State the blood parasite species.
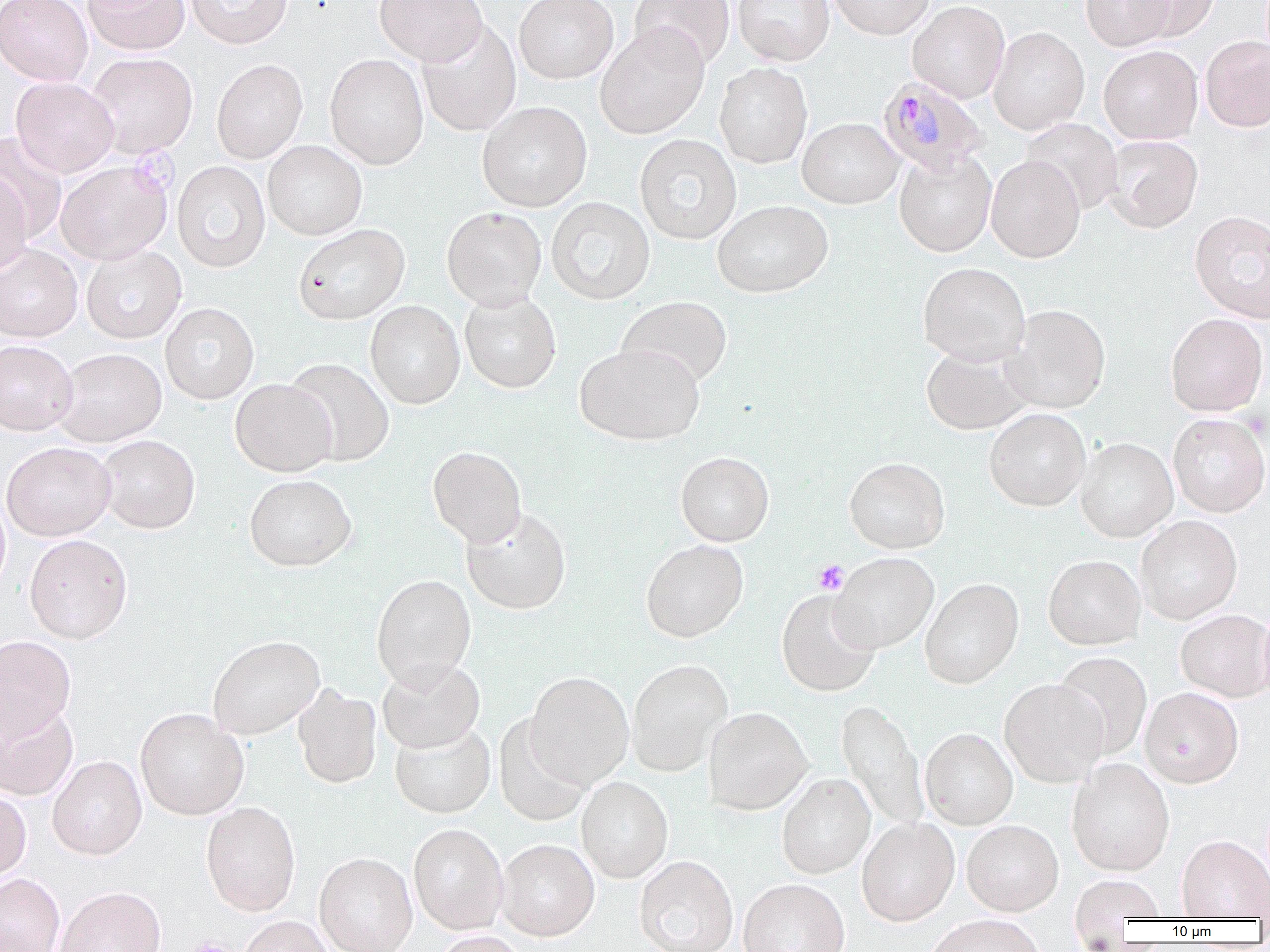

Plasmodium malariae.

Approximate bounding boxes as (x1,y1)-(x2,y2) corner pairs in pixels. Plasmodium malariae-infected red blood cell locations: (877,76)-(989,173). Uninfected red blood cell locations: (0,0)-(92,86), (83,0)-(190,55), (184,0)-(293,49), (374,0)-(488,66), (514,0)-(618,84), (630,0)-(735,70), (733,0)-(836,65), (828,0)-(934,39), (1081,0)-(1175,51), (1128,0)-(1219,42), (907,1)-(1010,104), (417,21)-(521,137), (595,25)-(709,139), (988,26)-(1089,135), (1200,35)-(1270,132), (1098,45)-(1203,144), (85,52)-(198,158), (324,54)-(429,169), (211,59)-(308,164), (714,62)-(813,169), (11,77)-(119,177), (477,101)-(592,211), (797,117)-(904,208), (1021,118)-(1123,215), (1,132)-(67,244), (634,134)-(742,245), (1103,135)-(1203,232), (262,140)-(367,240), (893,149)-(997,257), (985,155)-(1085,262), (56,161)-(172,265), (172,161)-(270,273), (0,171)-(32,277), (546,197)-(655,305), (712,200)-(833,298), (441,207)-(547,310), (1190,211)-(1270,323), (293,224)-(410,324), (0,244)-(83,342), (81,245)-(186,344), (918,262)-(1030,366), (460,291)-(562,393), (616,296)-(733,389), (365,300)-(465,409), (160,302)-(259,404), (1001,304)-(1111,413), (1165,313)-(1268,417), (0,340)-(78,435), (575,343)-(704,445), (921,345)-(1034,435), (54,348)-(166,447), (284,358)-(395,466), (229,379)-(337,477), (984,408)-(1091,511), (1168,413)-(1269,517), (96,434)-(200,533), (1076,437)-(1178,542), (1,442)-(116,540), (427,446)-(527,547), (675,451)-(774,547), (844,457)-(950,554), (244,475)-(357,572), (0,493)-(11,597), (461,506)-(572,615), (1135,515)-(1243,624), (24,534)-(133,643), (641,540)-(748,642), (830,553)-(939,653), (1043,555)-(1146,650), (371,574)-(476,690), (920,579)-(1023,688), (776,589)-(881,697), (1175,609)-(1270,702), (0,635)-(76,741), (208,635)-(325,740), (1053,651)-(1152,759), (377,658)-(485,753), (626,659)-(734,776), (525,671)-(634,788), (999,678)-(1109,788), (292,684)-(383,788), (1139,687)-(1244,788), (836,699)-(929,835), (0,701)-(79,801), (135,708)-(249,820), (704,708)-(811,815), (493,714)-(591,827), (389,720)-(495,819), (920,729)-(1018,829), (47,755)-(147,860), (1067,759)-(1174,876), (777,773)-(876,878), (576,777)-(673,883), (0,789)-(31,882), (201,801)-(301,916), (857,819)-(960,926), (961,821)-(1064,917), (408,823)-(509,934), (1177,834)-(1270,920), (497,839)-(599,940), (314,852)-(418,952), (634,856)-(738,952), (0,873)-(65,952), (1069,876)-(1165,928), (738,879)-(850,952), (54,886)-(166,952), (238,915)-(333,952), (924,916)-(1045,952), (430,931)-(529,952). Platelet locations: (813,560)-(849,595), (181,937)-(237,952). Image is 1270×952 pixels. 1000x magnification. Light microscopy. Thin blood smear. Single field of view.